Name the parasite shown.
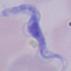

A trypanosome.

{
  "magnification": "1000x",
  "modality": "micrograph"
}